Report the malaria status of this cell.
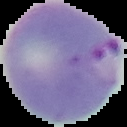

Parasitized.

The area outside the segmented cell region is set to black. From a thin blood smear. Image is 127×127 pixels.